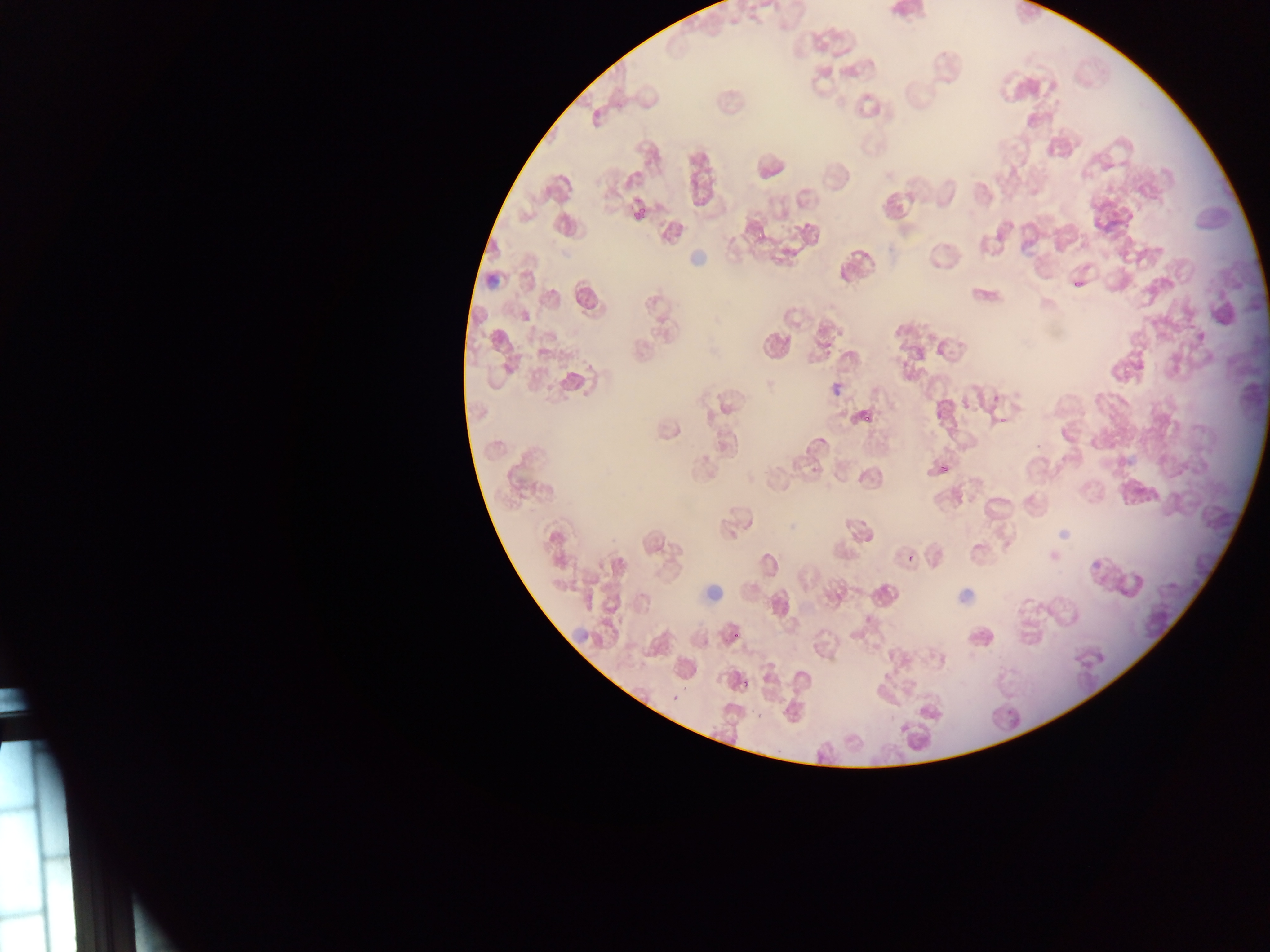
Approximate bounding boxes as {left, top, right, bottom} in pixels.
Summary:
  - Malaria parasite locations: {630, 202, 650, 225}, {1071, 273, 1084, 292}, {860, 402, 880, 426}, {940, 454, 959, 475}, {740, 665, 755, 686}
  - Preparation: thin blood smear
  - Capture: mobile-phone photograph through a microscope
  - Image size: 1270×952 pixels
  - Country: Ghana
  - Field of view: single